Classify this cell by malaria status.
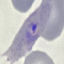
Parasitized.

preparation = thin blood smear
image type = cell patch, automatically extracted from a larger field of view and resized to 64 × 64 pixels
stain = Giemsa
capture = smartphone through the microscope eyepiece